Assess this cell for malaria.
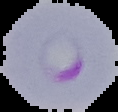

Parasitized.

Segmented cell region on a black background. From a thin blood film. Image is 118×112 pixels.